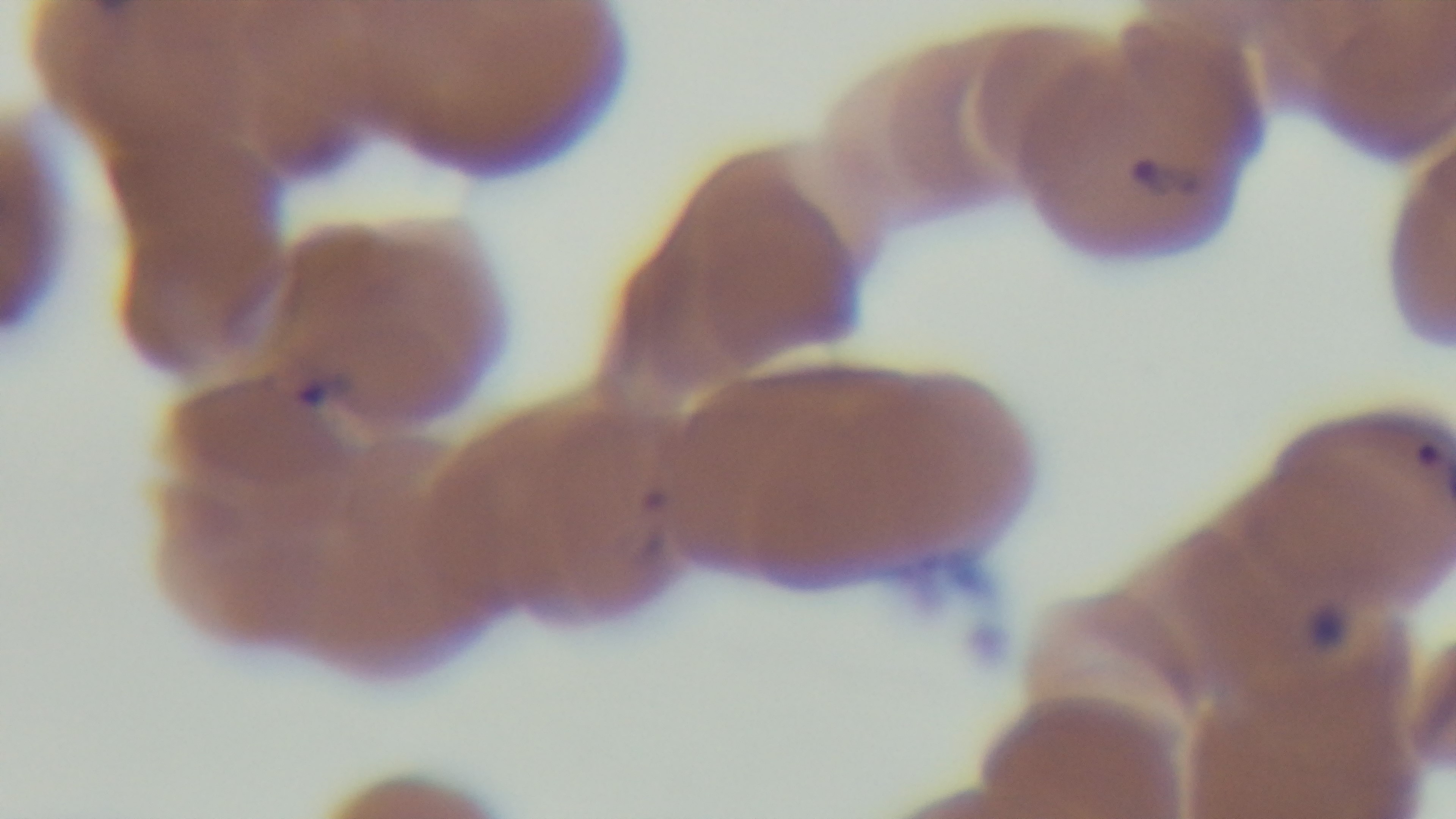
objective = 100x oil immersion
malaria status = infected
modality = light microscopy
stain = Giemsa
capture = mounted 4K digital camera
field of view = single
preparation = thin